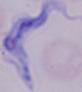

{
  "modality": "photomicrograph",
  "identification": "trypanosome",
  "magnification": "1000x"
}